Report the malaria status of this cell.
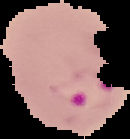
It is parasitized.

Image is 130×139 pixels. Cell region segmented out of the field of view; the surrounding area is masked to black. From a thin blood smear.